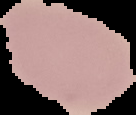
Summary:
  - Image size: 136×115 pixels
  - Image type: segmented cell region with the area outside set to black
  - Preparation: thin blood film
  - Malaria status: uninfected